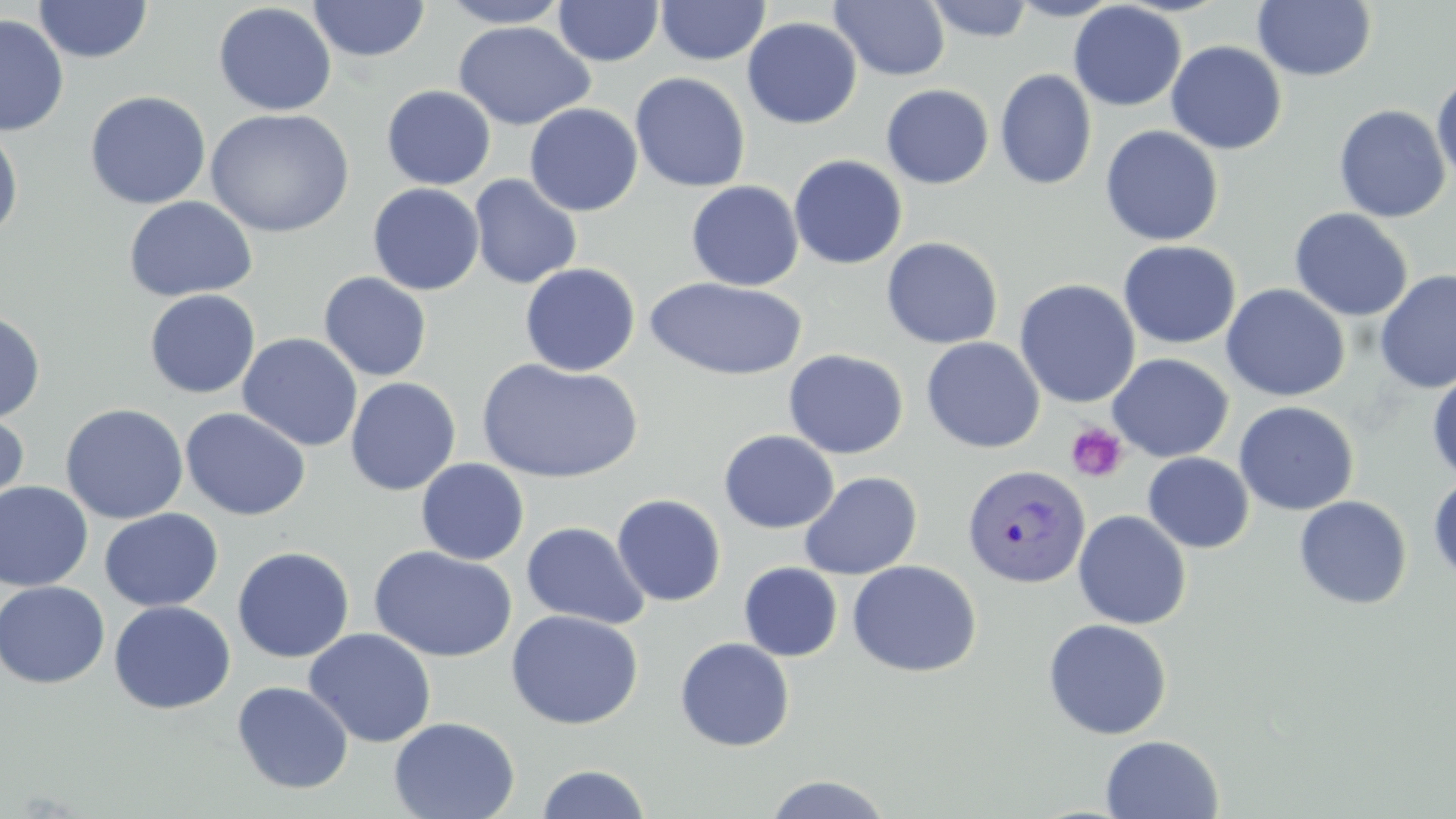

Summary:
  - Coordinate format: approximate bounding boxes as named x1/y1/x2/y2 corners in pixels
  - Uninfected red blood cell locations: (x1=33, y1=0, x2=153, y2=63), (x1=308, y1=0, x2=431, y2=62), (x1=437, y1=0, x2=574, y2=28), (x1=656, y1=0, x2=770, y2=65), (x1=830, y1=0, x2=950, y2=81), (x1=922, y1=0, x2=1036, y2=43), (x1=1007, y1=0, x2=1123, y2=21), (x1=552, y1=1, x2=663, y2=67), (x1=1252, y1=1, x2=1378, y2=82), (x1=213, y1=2, x2=337, y2=117), (x1=1068, y1=2, x2=1186, y2=111), (x1=0, y1=13, x2=69, y2=136), (x1=742, y1=17, x2=862, y2=129), (x1=455, y1=21, x2=595, y2=130), (x1=1166, y1=41, x2=1287, y2=154), (x1=995, y1=68, x2=1097, y2=190), (x1=630, y1=72, x2=751, y2=192), (x1=1431, y1=74, x2=1456, y2=187), (x1=881, y1=84, x2=994, y2=189), (x1=381, y1=85, x2=496, y2=190), (x1=84, y1=90, x2=211, y2=210), (x1=524, y1=103, x2=643, y2=216), (x1=1333, y1=104, x2=1451, y2=223), (x1=205, y1=108, x2=355, y2=238), (x1=0, y1=125, x2=24, y2=241), (x1=1100, y1=125, x2=1224, y2=246), (x1=788, y1=154, x2=908, y2=270), (x1=468, y1=174, x2=583, y2=289), (x1=686, y1=180, x2=804, y2=291), (x1=367, y1=183, x2=484, y2=296), (x1=123, y1=196, x2=258, y2=302), (x1=1289, y1=208, x2=1413, y2=322), (x1=881, y1=237, x2=1003, y2=350), (x1=1118, y1=240, x2=1241, y2=350), (x1=520, y1=262, x2=641, y2=376), (x1=1374, y1=269, x2=1456, y2=394), (x1=328, y1=271, x2=442, y2=490), (x1=318, y1=272, x2=432, y2=381), (x1=644, y1=277, x2=808, y2=381), (x1=1014, y1=278, x2=1141, y2=408), (x1=1221, y1=283, x2=1350, y2=402), (x1=144, y1=289, x2=262, y2=399), (x1=0, y1=309, x2=46, y2=424), (x1=237, y1=333, x2=363, y2=452), (x1=921, y1=337, x2=1045, y2=453), (x1=783, y1=349, x2=909, y2=460), (x1=1107, y1=353, x2=1234, y2=463), (x1=1127, y1=354, x2=1244, y2=557), (x1=477, y1=358, x2=643, y2=484), (x1=1427, y1=370, x2=1456, y2=484), (x1=345, y1=377, x2=461, y2=496), (x1=1234, y1=401, x2=1359, y2=516), (x1=60, y1=403, x2=189, y2=524), (x1=0, y1=407, x2=30, y2=518), (x1=180, y1=407, x2=311, y2=521), (x1=719, y1=430, x2=839, y2=534), (x1=1142, y1=452, x2=1254, y2=553), (x1=415, y1=458, x2=529, y2=565), (x1=799, y1=472, x2=923, y2=580), (x1=1428, y1=474, x2=1456, y2=586), (x1=0, y1=480, x2=94, y2=592), (x1=611, y1=494, x2=727, y2=607), (x1=1294, y1=496, x2=1412, y2=610), (x1=100, y1=508, x2=223, y2=612), (x1=1073, y1=509, x2=1192, y2=630), (x1=521, y1=521, x2=650, y2=630), (x1=232, y1=546, x2=355, y2=663), (x1=368, y1=546, x2=517, y2=663), (x1=847, y1=559, x2=982, y2=678), (x1=739, y1=563, x2=842, y2=661), (x1=0, y1=580, x2=110, y2=689), (x1=108, y1=600, x2=236, y2=715), (x1=506, y1=609, x2=644, y2=729), (x1=1042, y1=618, x2=1173, y2=740), (x1=304, y1=628, x2=437, y2=747), (x1=675, y1=637, x2=795, y2=752), (x1=232, y1=681, x2=354, y2=794), (x1=388, y1=716, x2=520, y2=819), (x1=1100, y1=734, x2=1224, y2=818), (x1=535, y1=763, x2=653, y2=819), (x1=762, y1=774, x2=894, y2=818)
  - Plasmodium vivax-infected red blood cell locations: (x1=962, y1=463, x2=1091, y2=588)
  - Platelet locations: (x1=1065, y1=421, x2=1129, y2=483)
  - Slide-level diagnosis: Plasmodium vivax
  - Field of view: one of a larger specimen
  - Magnification: 1000x
  - Stain: May-Grünwald-Giemsa
  - Modality: optical microscopy
  - Preparation: thin blood film
  - Image size: 1456×819 pixels